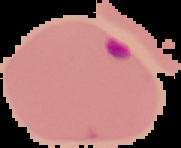

Summary:
  - Image size: 181×148 pixels
  - Image type: segmented cell region with the area outside set to black
  - Preparation: thin blood smear
  - Malaria status: parasitized